Locate every leukocyte (white blood cell).
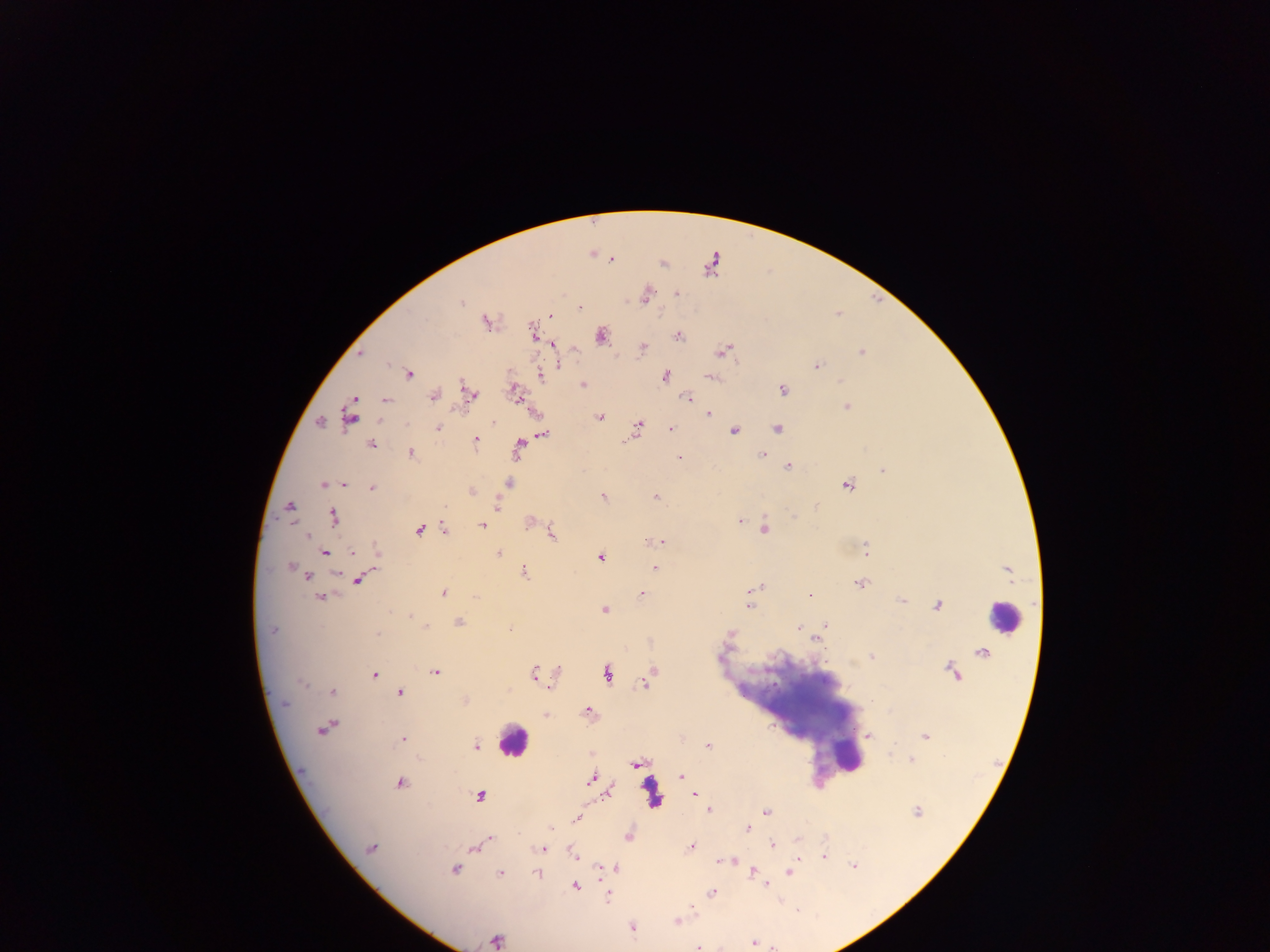
Approximate centers as (x, y) in pixels.
Leukocytes: (1002, 618), (511, 742), (844, 753).

Malaria parasite locations: (611, 259), (662, 264), (712, 266), (676, 293), (645, 295), (461, 302), (580, 308), (550, 315), (486, 322), (534, 333), (601, 335), (678, 336), (553, 344), (642, 349), (723, 350), (861, 352), (361, 353), (559, 365), (818, 366), (409, 374), (540, 376), (664, 376), (711, 377), (583, 384), (466, 387), (782, 389), (514, 390), (470, 393), (433, 396), (355, 398), (688, 398), (386, 400), (846, 407), (708, 413), (350, 416), (600, 417), (493, 421), (320, 422), (637, 425), (438, 428), (777, 428), (670, 429), (734, 430), (543, 435), (633, 435), (476, 438), (370, 444), (519, 444), (411, 453), (762, 454), (679, 458), (788, 466), (883, 470), (344, 483), (323, 484), (509, 484), (847, 485), (372, 489), (472, 492), (603, 496), (655, 497), (497, 505), (290, 506), (793, 516), (333, 517), (739, 522), (529, 523), (482, 525), (444, 529), (764, 529), (418, 530), (552, 533), (307, 535), (663, 542), (865, 548), (377, 552), (325, 553), (353, 553), (499, 554), (601, 557), (290, 566), (654, 569), (336, 573), (524, 573), (307, 577), (359, 580), (860, 584), (755, 587), (443, 593), (641, 594), (320, 596), (810, 596), (902, 601), (749, 606), (937, 606), (604, 610), (410, 616), (459, 622), (825, 624), (425, 627), (798, 627), (510, 629), (272, 630), (730, 633), (377, 634), (817, 638), (872, 657), (558, 671), (534, 672), (436, 673), (650, 673), (373, 674), (607, 674), (644, 682), (303, 683), (550, 687), (332, 691), (400, 692), (465, 701), (285, 704), (588, 712), (545, 715), (329, 725), (323, 729), (869, 736), (925, 737), (402, 739), (476, 746), (708, 746), (912, 760), (634, 764), (681, 776), (591, 779), (400, 783), (610, 792), (694, 795), (480, 796), (709, 810), (766, 812), (917, 812), (577, 818), (748, 828), (628, 837), (490, 838), (797, 840), (772, 844), (692, 847), (370, 848), (475, 849), (541, 849), (823, 856), (574, 857), (722, 861), (734, 861), (853, 865), (616, 867), (600, 868), (455, 870), (752, 871), (790, 873), (500, 874), (537, 874), (767, 885), (576, 887), (712, 893), (608, 897), (676, 920), (632, 928), (496, 940), (753, 943), (698, 948). Thick blood smear. Photographed through a microscope with a mobile-phone camera. Image is 1270×952 pixels. Single field of view. Collected in Ghana.